Point out each malaria parasite.
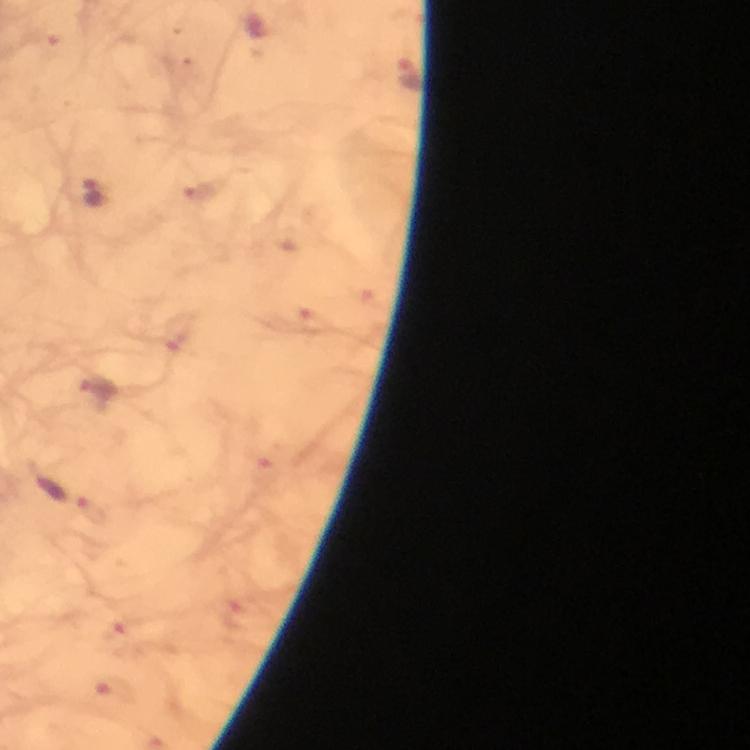
Approximate centers as [x, y] in pixels.
Malaria parasites: [410, 77], [93, 196], [177, 335], [96, 391], [95, 512], [235, 615], [119, 636], [121, 693].

Summary:
  - Context: from a malaria diagnostic workup
  - Magnification: 100x
  - Stain: Giemsa
  - Capture: smartphone camera through the microscope
  - Immersion oil: applied
  - Image size: 750×750 pixels
  - Cropped from: a single field of view
  - Preparation: thick blood film